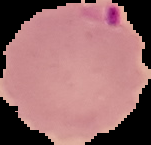

Summary:
  - Result: Plasmodium parasites detected
  - Image size: 151×145 pixels
  - Preparation: thin blood smear
  - Image type: cell region segmented out of the field of view; surrounding area masked to black